Name the parasite shown.
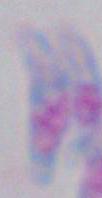
Toxoplasma gondii.

Summary:
  - Magnification: 1000x
  - Modality: photomicrograph